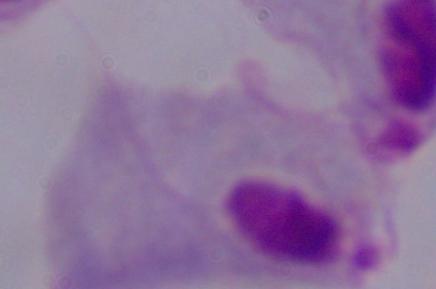

Micrograph. A trichomonad is seen. Captured at 1000x magnification.